State which parasite is depicted.
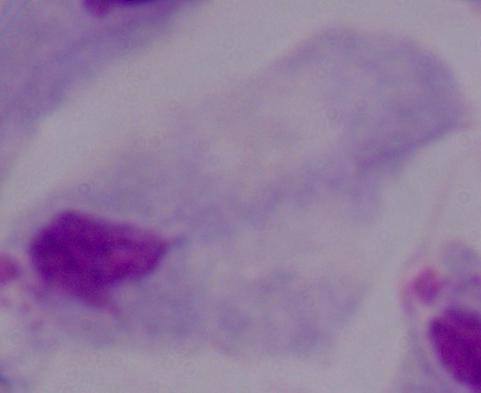
This is a trichomonad.

modality: micrograph
magnification: 1000x